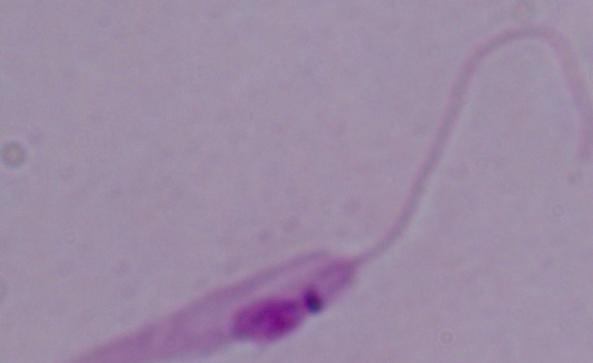
Photomicrograph. A Leishmania parasite is shown. Captured at 1000x magnification.